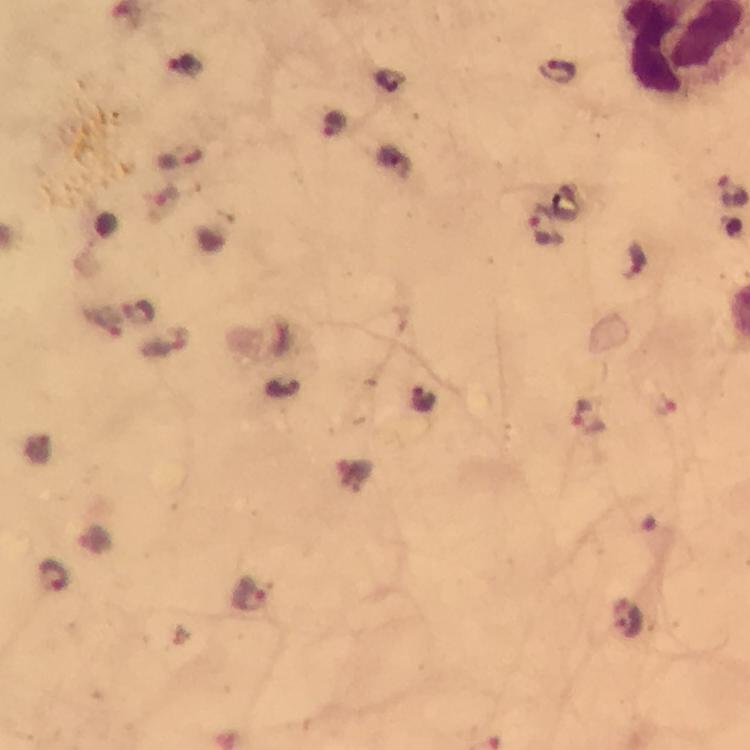 Approximate object centers, in pixels from the top-left corner. Malaria parasite locations: (x=185, y=66), (x=559, y=72), (x=335, y=126), (x=544, y=224), (x=588, y=418), (x=56, y=576), (x=251, y=598). Cropped region of a single field of view. Image is 750×750 pixels. From a malaria diagnostic workup. 100x magnification. Photographed through the microscope with a smartphone camera. Giemsa stain. Immersion oil applied. Thick blood film.